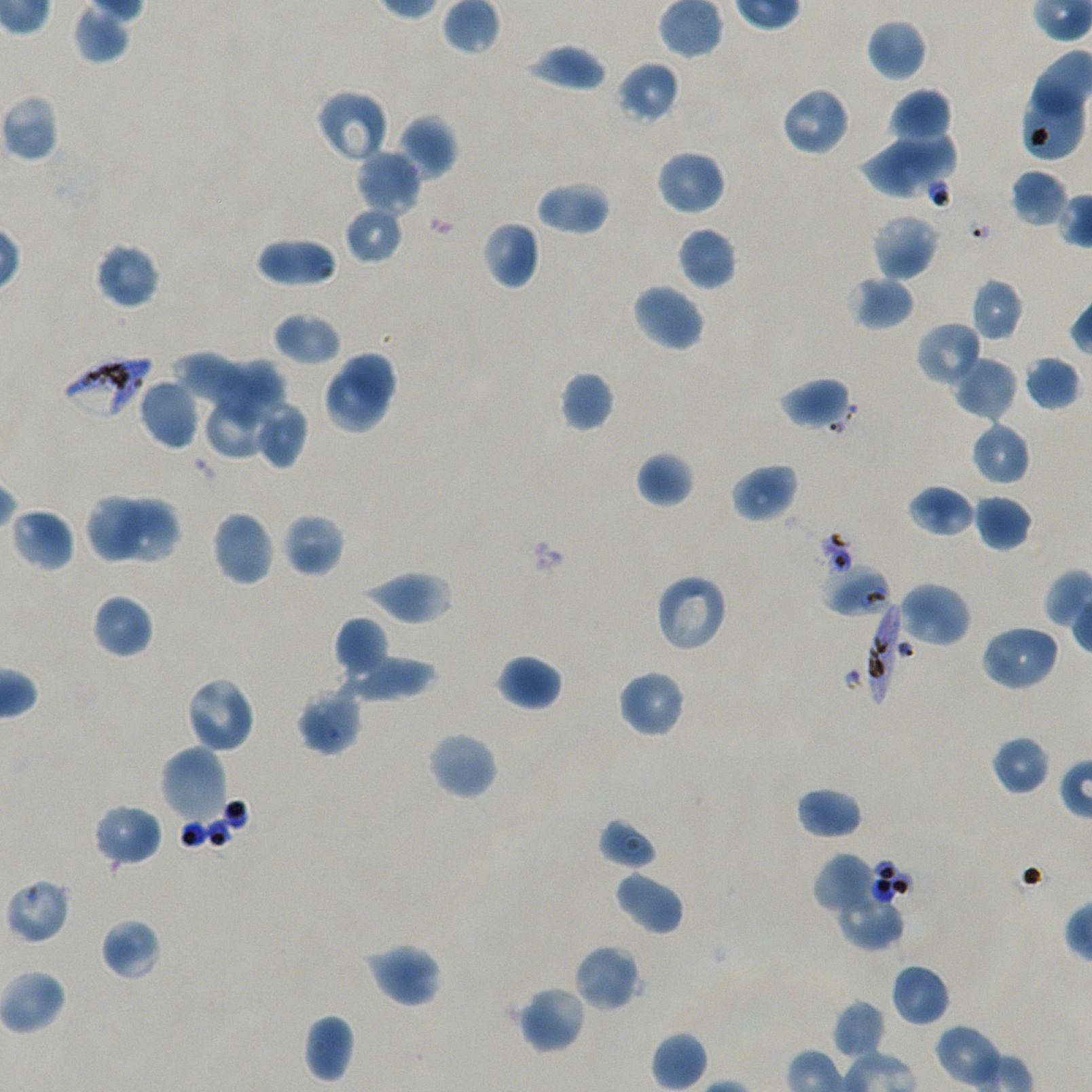
Approximate bounding boxes as {x1, y1, x2, y2} in pixels. Not every red blood cell is marked. Locations of uninfected red blood cells: {441, 0, 500, 54}, {71, 3, 130, 66}, {866, 18, 928, 82}, {524, 43, 607, 94}, {615, 60, 680, 125}, {1022, 83, 1089, 162}, {781, 86, 851, 157}, {314, 88, 389, 164}, {888, 88, 952, 146}, {0, 94, 60, 163}, {398, 114, 458, 179}, {890, 122, 959, 181}, {861, 141, 939, 200}, {354, 149, 422, 217}, {655, 149, 727, 216}, {1009, 169, 1068, 228}, {535, 181, 610, 236}, {342, 206, 404, 266}, {870, 213, 941, 280}, {482, 219, 541, 289}, {677, 226, 738, 291}, {255, 236, 338, 288}, {94, 241, 161, 310}, {848, 274, 916, 331}, {970, 277, 1024, 343}, {631, 282, 706, 352}, {272, 312, 342, 367}, {915, 321, 983, 388}, {338, 350, 398, 412}, {169, 352, 252, 414}, {1021, 355, 1080, 412}, {951, 356, 1018, 422}, {216, 357, 290, 429}, {326, 369, 392, 433}, {558, 370, 616, 433}, {778, 376, 853, 432}, {137, 378, 200, 450}, {202, 393, 272, 460}, {253, 402, 309, 470}, {970, 419, 1032, 486}, {635, 450, 695, 508}, {730, 462, 799, 523}, {906, 484, 975, 538}, {86, 493, 143, 564}, {973, 494, 1034, 551}, {115, 498, 181, 565}, {10, 506, 75, 572}, {211, 510, 275, 587}, {282, 513, 346, 577}, {359, 570, 454, 625}, {654, 572, 729, 654}, {898, 582, 971, 648}, {90, 594, 154, 659}, {333, 616, 390, 679}, {979, 623, 1061, 692}, {494, 653, 563, 712}, {340, 654, 439, 703}, {615, 668, 686, 739}, {184, 676, 256, 754}, {295, 685, 363, 756}, {426, 730, 499, 801}, {989, 734, 1052, 796}, {159, 744, 230, 825}, {795, 786, 864, 841}, {93, 803, 163, 867}, {597, 818, 659, 871}, {812, 853, 879, 917}, {614, 869, 685, 935}, {4, 878, 71, 945}, {835, 892, 905, 951}, {100, 918, 161, 979}, {363, 941, 444, 1008}, {573, 943, 642, 1012}, {890, 962, 951, 1027}, {0, 969, 67, 1035}, {517, 985, 588, 1055}, {831, 999, 886, 1061}, {303, 1013, 355, 1084}, {650, 1030, 708, 1091}. Locations of red blood cells of indeterminate infection status: {824, 566, 893, 617}. Locations of infected red blood cells: {60, 352, 151, 420}, {864, 599, 909, 707}. Giemsa stain. One field from this slide. Thin blood smear. 100x objective under oil immersion, numerical aperture 1.45. Plasmodium falciparum strain NF54 in static in-vitro culture. Blood group of the donor: A+/O+. Image is 1092×1092 pixels.